Report the malaria status of this cell.
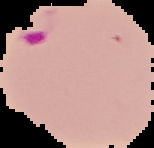

Parasitized.

{
  "preparation": "thin blood film",
  "image_size": "154×148 pixels",
  "image_type": "cell region segmented out of the field of view; surrounding area masked to black"
}